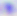

Toxoplasma gondii is shown. Micrograph. 400x magnification.